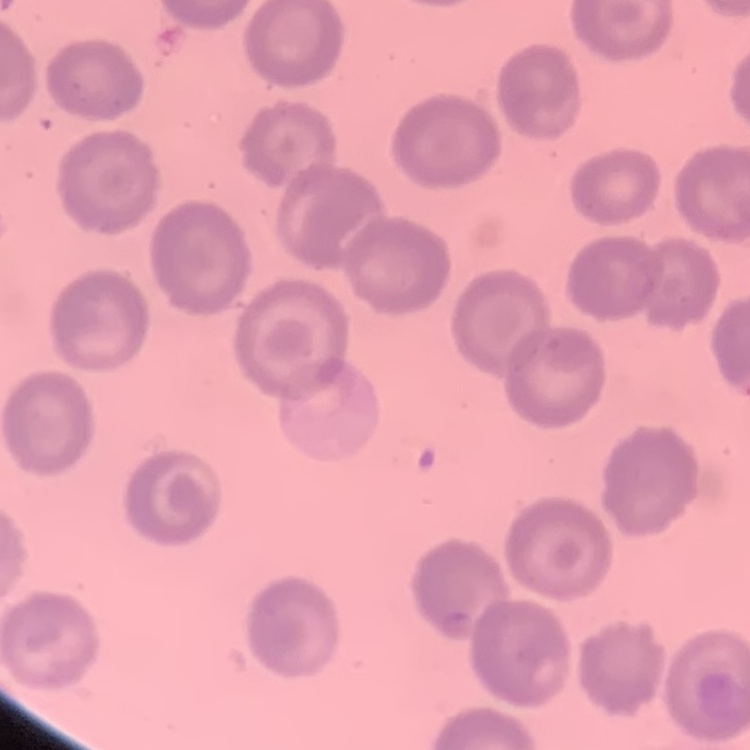
Summary:
  - Erythrocyte morphology: no rouleaux formation
  - Image type: square crop of a larger photomicrograph
  - Preparation: thin blood film
  - Stain: Field's or Giemsa